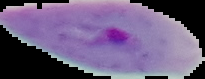

Summary:
  - Image type: segmented cell region on a black background
  - Image size: 205×79 pixels
  - Preparation: thin blood smear
  - Result: Plasmodium parasites detected